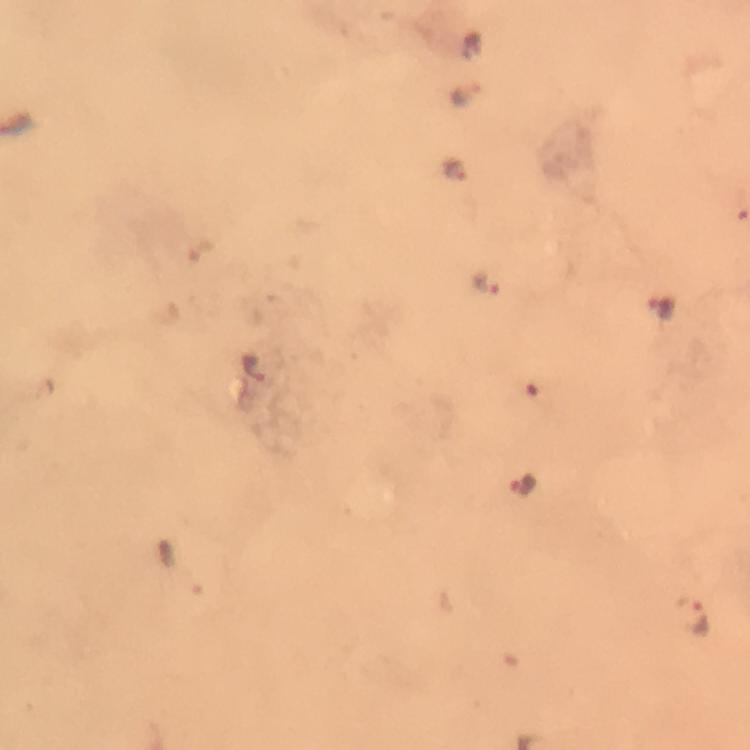

context = from a diagnostic examination for malaria
capture = smartphone camera through the microscope
magnification = 100x
Plasmodium parasite locations = approximate centers as {x, y} in pixels: {465, 92}, {455, 169}, {487, 283}, {661, 309}, {523, 488}, {689, 617}
stain = Giemsa
preparation = thick blood smear
cropped from = a single field of view
image size = 750×750 pixels
immersion oil = used